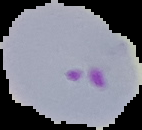
Summary:
  - Preparation: thin blood film
  - Image type: segmented cell region on a black background
  - Image size: 142×130 pixels
  - Malaria status: parasitized